Assess this cell for malaria.
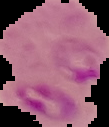

It is parasitized.

image size = 109×127 pixels
image type = cell region segmented out of the field of view; surrounding area masked to black
preparation = thin blood film